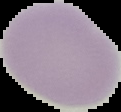 Image is 121×112 pixels. Malaria status: uninfected. From a thin blood smear. Cell region segmented out of the field of view; the surrounding area is masked to black.